State the blood parasite species.
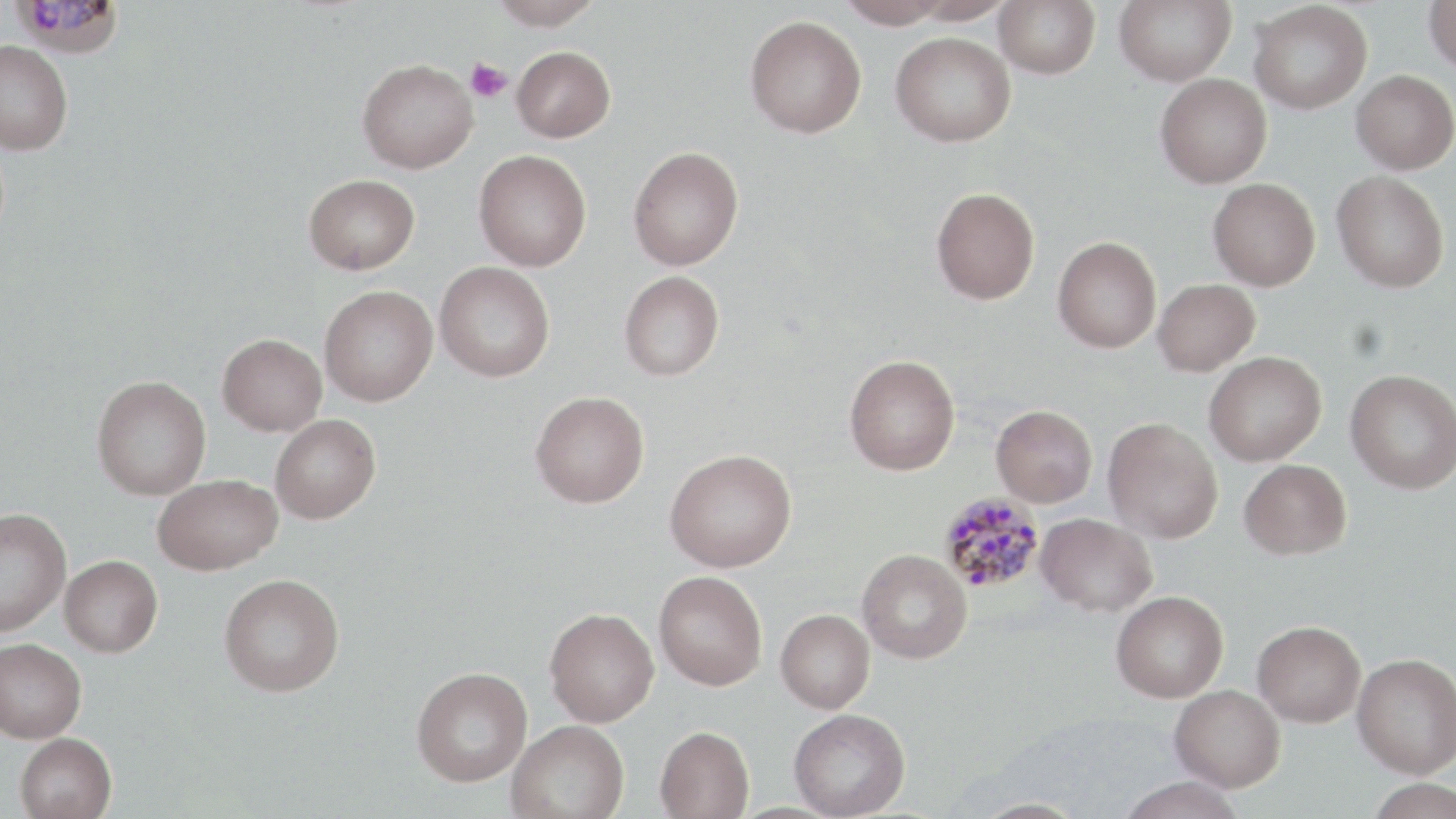
Plasmodium malariae.

field_of_view: one of a larger specimen
plasmodium_malariae_infected_red_blood_cell_locations: 'approximate bounding boxes as named x1/y1/x2/y2 corners in pixels: (x1=13, y1=0, x2=126, y2=58), (x1=939, y1=492, x2=1045, y2=593)'
image_size: 1456×819 pixels
magnification: 1000x
preparation: thin blood film
modality: light microscopy
uninfected_red_blood_cell_locations: 'approximate bounding boxes as named x1/y1/x2/y2 corners in pixels: (x1=489, y1=0, x2=603, y2=29), (x1=836, y1=0, x2=954, y2=28), (x1=994, y1=0, x2=1100, y2=79), (x1=1114, y1=0, x2=1236, y2=85), (x1=1249, y1=1, x2=1372, y2=114), (x1=1424, y1=1, x2=1456, y2=77), (x1=745, y1=14, x2=867, y2=137), (x1=890, y1=32, x2=1016, y2=147), (x1=0, y1=40, x2=73, y2=155), (x1=511, y1=46, x2=616, y2=142), (x1=357, y1=58, x2=478, y2=173), (x1=1351, y1=70, x2=1456, y2=174), (x1=1155, y1=73, x2=1272, y2=188), (x1=628, y1=146, x2=744, y2=270), (x1=474, y1=149, x2=592, y2=271), (x1=1332, y1=170, x2=1449, y2=292), (x1=303, y1=173, x2=420, y2=274), (x1=1208, y1=178, x2=1320, y2=291), (x1=931, y1=187, x2=1040, y2=304), (x1=1053, y1=237, x2=1161, y2=353), (x1=434, y1=262, x2=555, y2=382), (x1=619, y1=271, x2=725, y2=381), (x1=1153, y1=279, x2=1260, y2=376), (x1=319, y1=285, x2=438, y2=406), (x1=217, y1=333, x2=327, y2=436), (x1=1204, y1=352, x2=1327, y2=466), (x1=844, y1=354, x2=960, y2=475), (x1=1345, y1=370, x2=1456, y2=494), (x1=92, y1=375, x2=211, y2=499), (x1=530, y1=391, x2=649, y2=507), (x1=991, y1=404, x2=1097, y2=506), (x1=270, y1=414, x2=381, y2=523), (x1=1103, y1=418, x2=1222, y2=543), (x1=665, y1=448, x2=796, y2=572), (x1=1239, y1=458, x2=1351, y2=559), (x1=152, y1=474, x2=282, y2=575), (x1=0, y1=506, x2=71, y2=637), (x1=1036, y1=513, x2=1157, y2=616), (x1=857, y1=548, x2=972, y2=663), (x1=59, y1=554, x2=162, y2=657), (x1=654, y1=570, x2=768, y2=690), (x1=219, y1=573, x2=344, y2=696), (x1=1111, y1=590, x2=1228, y2=702), (x1=544, y1=607, x2=659, y2=726), (x1=776, y1=609, x2=875, y2=713), (x1=1253, y1=620, x2=1366, y2=726), (x1=0, y1=638, x2=86, y2=742), (x1=1352, y1=652, x2=1456, y2=778), (x1=411, y1=666, x2=533, y2=786), (x1=1170, y1=684, x2=1285, y2=791), (x1=788, y1=708, x2=910, y2=818), (x1=506, y1=718, x2=629, y2=819), (x1=655, y1=725, x2=754, y2=819), (x1=15, y1=733, x2=117, y2=819), (x1=1115, y1=776, x2=1247, y2=819), (x1=1363, y1=778, x2=1456, y2=819), (x1=969, y1=798, x2=1090, y2=818)'
stain: May-Grünwald-Giemsa
platelet_locations: 'approximate bounding boxes as named x1/y1/x2/y2 corners in pixels: (x1=466, y1=57, x2=513, y2=103)'